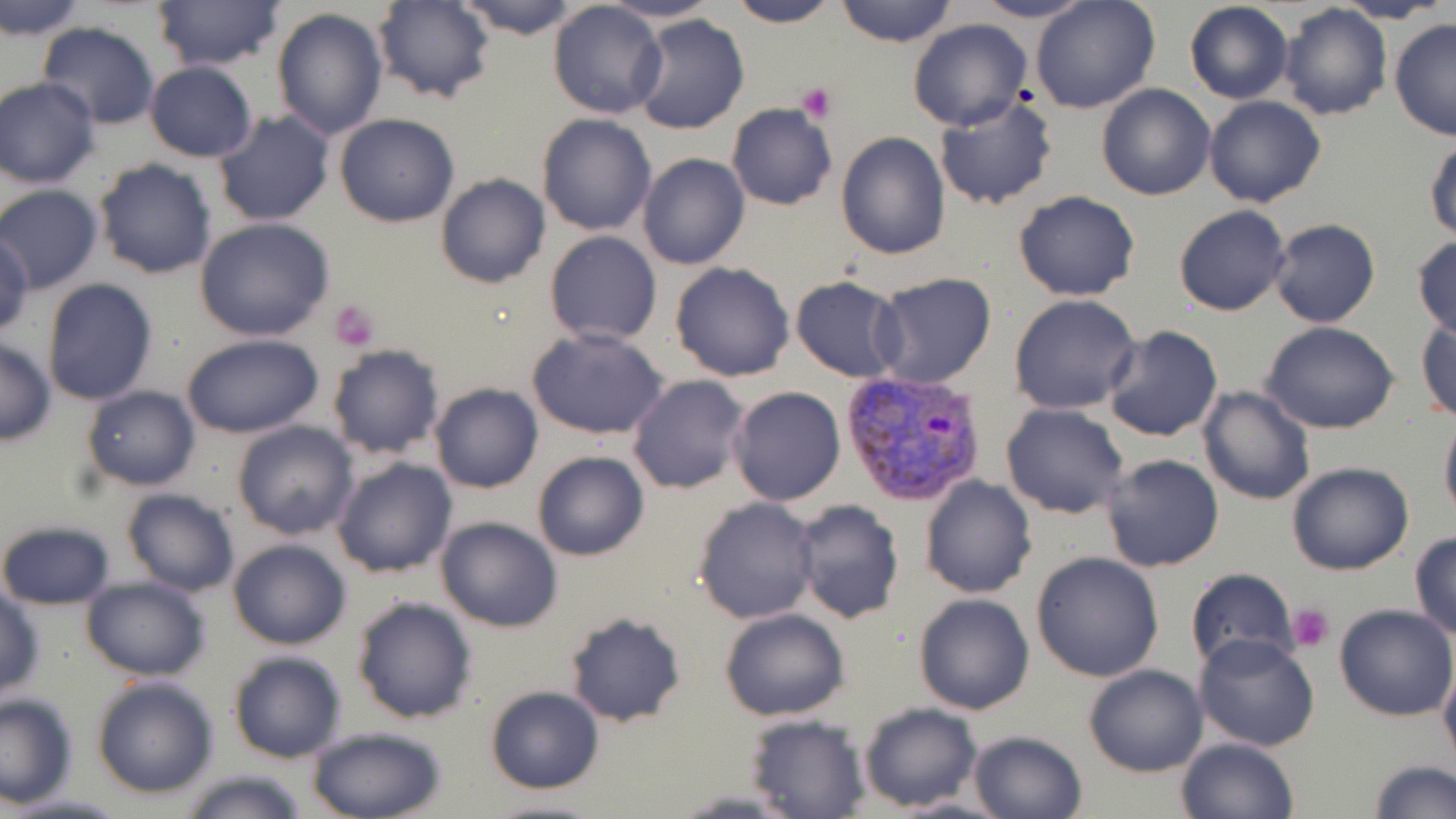

{
  "slide_level_diagnosis": "Plasmodium vivax",
  "field_of_view": "one of a larger specimen",
  "stain": "May-Grünwald-Giemsa",
  "plasmodium_vivax_infected_red_blood_cell_locations": "approximate bounding boxes as (x1, y1, x2, y2) in pixels: (837, 367, 989, 506)",
  "preparation": "thin blood smear",
  "platelet_locations": "approximate bounding boxes as (x1, y1, x2, y2) in pixels: (797, 82, 836, 123), (330, 299, 381, 351), (1288, 602, 1335, 651)",
  "image_size": "1456×819 pixels",
  "modality": "optical microscopy",
  "magnification": "1000x",
  "uninfected_red_blood_cell_locations": "approximate bounding boxes as (x1, y1, x2, y2) in pixels: (452, 0, 586, 40), (726, 0, 841, 27), (835, 0, 958, 48), (969, 0, 1097, 24), (1030, 0, 1161, 115), (150, 1, 284, 71), (372, 1, 495, 105), (602, 1, 722, 24), (1184, 1, 1293, 105), (1336, 1, 1449, 24), (1, 2, 89, 39), (548, 2, 668, 118), (1278, 4, 1391, 122), (272, 6, 389, 140), (630, 13, 748, 135), (907, 18, 1032, 132), (1389, 18, 1456, 140), (36, 22, 162, 129), (143, 62, 259, 161), (1, 76, 99, 187), (1097, 84, 1216, 200), (934, 93, 1059, 212), (1204, 95, 1325, 208), (727, 103, 836, 210), (213, 110, 335, 229), (333, 113, 460, 227), (535, 113, 657, 236), (835, 131, 952, 259), (1426, 139, 1456, 241), (636, 152, 750, 270), (94, 159, 216, 280), (435, 173, 550, 289), (0, 184, 104, 294), (1013, 190, 1140, 303), (1173, 204, 1291, 316), (193, 217, 336, 341), (1267, 218, 1380, 328), (544, 231, 663, 345), (1, 233, 34, 335), (1411, 234, 1456, 339), (669, 263, 794, 382), (871, 273, 998, 390), (790, 276, 907, 381), (42, 278, 159, 405), (1009, 293, 1142, 415), (1417, 317, 1456, 422), (1259, 320, 1399, 434), (1101, 325, 1223, 442), (529, 328, 670, 440), (181, 333, 327, 440), (0, 337, 57, 445), (326, 344, 447, 460), (626, 374, 750, 495), (430, 383, 543, 494), (81, 385, 200, 491), (728, 386, 845, 506), (1196, 386, 1316, 506), (1001, 403, 1130, 519), (1439, 408, 1456, 522), (231, 419, 358, 540), (532, 452, 648, 561), (1098, 453, 1223, 573), (331, 457, 457, 578), (1285, 460, 1415, 577), (919, 475, 1037, 598), (119, 489, 240, 597), (693, 496, 821, 625), (793, 499, 905, 623), (435, 516, 563, 633), (1, 518, 114, 611), (1409, 529, 1456, 639), (227, 537, 354, 651), (1031, 551, 1166, 683), (1183, 568, 1298, 676), (81, 575, 211, 682), (0, 585, 44, 701), (912, 593, 1034, 715), (350, 595, 478, 723), (1333, 604, 1455, 720), (718, 608, 849, 720), (563, 611, 689, 728), (1194, 631, 1321, 750), (227, 649, 349, 764), (1438, 657, 1456, 777), (1084, 664, 1208, 778), (89, 675, 219, 800), (484, 685, 606, 795), (0, 693, 77, 806), (858, 703, 982, 811), (744, 714, 871, 819), (303, 726, 449, 818), (967, 729, 1089, 819), (1175, 736, 1300, 819), (1365, 760, 1454, 817), (173, 768, 313, 819), (5, 792, 128, 817), (478, 796, 608, 818)"
}